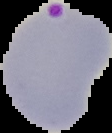
preparation = thin blood smear
image type = segmented cell region with the area outside set to black
image size = 112×133 pixels
malaria status = parasitized